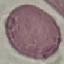
Malaria status: uninfected. Acquired by smartphone through the microscope eyepiece. Automatically extracted cell patch, resized to 64 × 64 pixels. Giemsa-stained preparation. Thin smear of blood.